Assess this cell for malaria.
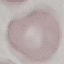

It is uninfected.

stain = Giemsa
preparation = thin blood smear
capture = smartphone camera at the microscope eyepiece
image type = cell patch, automatically extracted from a larger field of view and resized to 64 × 64 pixels